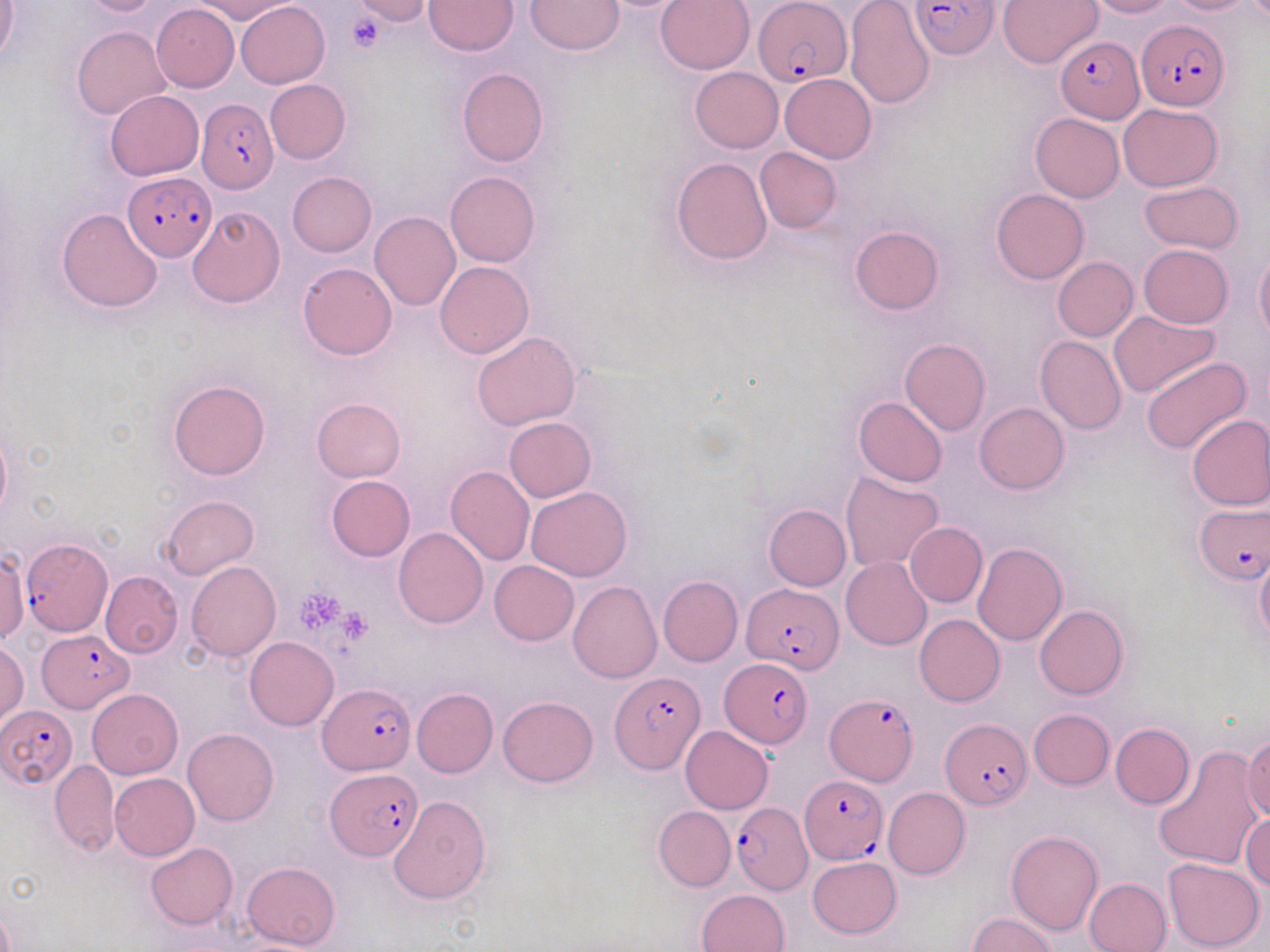

Summary:
  - Coordinate format: approximate bounding boxes as named x1/y1/x2/y2 corners in pixels
  - Platelet locations: (x1=346, y1=11, x2=389, y2=51), (x1=298, y1=591, x2=348, y2=633), (x1=336, y1=609, x2=374, y2=643)
  - Plasmodium falciparum-infected red blood cell locations: (x1=754, y1=1, x2=851, y2=88), (x1=911, y1=1, x2=999, y2=60), (x1=1135, y1=19, x2=1228, y2=113), (x1=1056, y1=36, x2=1142, y2=123), (x1=197, y1=97, x2=277, y2=194), (x1=124, y1=171, x2=217, y2=259), (x1=1194, y1=504, x2=1268, y2=583), (x1=20, y1=538, x2=113, y2=637), (x1=742, y1=582, x2=843, y2=671), (x1=39, y1=631, x2=132, y2=712), (x1=719, y1=658, x2=812, y2=749), (x1=610, y1=672, x2=704, y2=772), (x1=319, y1=682, x2=413, y2=774), (x1=825, y1=693, x2=917, y2=786), (x1=3, y1=705, x2=77, y2=786), (x1=941, y1=718, x2=1031, y2=809), (x1=326, y1=768, x2=421, y2=858), (x1=799, y1=775, x2=888, y2=864), (x1=730, y1=802, x2=812, y2=895)
  - Uninfected red blood cell locations: (x1=75, y1=0, x2=163, y2=16), (x1=193, y1=0, x2=298, y2=22), (x1=347, y1=0, x2=432, y2=26), (x1=425, y1=0, x2=518, y2=55), (x1=526, y1=0, x2=623, y2=54), (x1=656, y1=0, x2=754, y2=74), (x1=845, y1=0, x2=933, y2=107), (x1=1085, y1=0, x2=1178, y2=18), (x1=1164, y1=0, x2=1257, y2=15), (x1=998, y1=1, x2=1102, y2=70), (x1=236, y1=2, x2=330, y2=88), (x1=0, y1=3, x2=20, y2=63), (x1=151, y1=3, x2=239, y2=91), (x1=72, y1=26, x2=171, y2=121), (x1=689, y1=67, x2=783, y2=153), (x1=457, y1=68, x2=548, y2=166), (x1=781, y1=74, x2=876, y2=163), (x1=264, y1=79, x2=350, y2=164), (x1=105, y1=90, x2=204, y2=180), (x1=1118, y1=104, x2=1222, y2=191), (x1=1030, y1=112, x2=1124, y2=201), (x1=755, y1=147, x2=841, y2=232), (x1=671, y1=157, x2=773, y2=264), (x1=287, y1=171, x2=376, y2=256), (x1=445, y1=171, x2=540, y2=267), (x1=1138, y1=180, x2=1245, y2=253), (x1=991, y1=188, x2=1089, y2=285), (x1=187, y1=205, x2=284, y2=308), (x1=57, y1=207, x2=164, y2=312), (x1=371, y1=211, x2=461, y2=311), (x1=849, y1=226, x2=943, y2=315), (x1=1139, y1=245, x2=1233, y2=329), (x1=1255, y1=250, x2=1270, y2=346), (x1=1052, y1=257, x2=1139, y2=341), (x1=435, y1=261, x2=534, y2=357), (x1=297, y1=263, x2=396, y2=360), (x1=1109, y1=311, x2=1220, y2=398), (x1=472, y1=332, x2=582, y2=430), (x1=1036, y1=334, x2=1127, y2=435), (x1=899, y1=338, x2=992, y2=435), (x1=1141, y1=357, x2=1252, y2=454), (x1=168, y1=379, x2=269, y2=480), (x1=853, y1=396, x2=948, y2=486), (x1=312, y1=398, x2=406, y2=482), (x1=975, y1=402, x2=1069, y2=494), (x1=1185, y1=414, x2=1270, y2=512), (x1=505, y1=417, x2=595, y2=501), (x1=0, y1=425, x2=11, y2=522), (x1=445, y1=465, x2=534, y2=565), (x1=839, y1=471, x2=944, y2=572), (x1=325, y1=475, x2=415, y2=562), (x1=526, y1=486, x2=632, y2=581), (x1=161, y1=495, x2=257, y2=578), (x1=763, y1=504, x2=850, y2=590), (x1=904, y1=522, x2=987, y2=607), (x1=393, y1=527, x2=488, y2=628), (x1=974, y1=542, x2=1067, y2=646), (x1=1, y1=549, x2=30, y2=643), (x1=1255, y1=551, x2=1270, y2=647), (x1=841, y1=556, x2=932, y2=649), (x1=489, y1=560, x2=579, y2=646), (x1=186, y1=561, x2=281, y2=660), (x1=100, y1=571, x2=183, y2=658), (x1=657, y1=576, x2=743, y2=666), (x1=568, y1=580, x2=662, y2=683), (x1=1034, y1=605, x2=1128, y2=699), (x1=914, y1=614, x2=1005, y2=706), (x1=245, y1=636, x2=338, y2=730), (x1=0, y1=640, x2=29, y2=729), (x1=411, y1=688, x2=497, y2=778), (x1=87, y1=689, x2=183, y2=779), (x1=497, y1=696, x2=598, y2=787), (x1=1028, y1=708, x2=1114, y2=789), (x1=1110, y1=723, x2=1194, y2=809), (x1=680, y1=725, x2=773, y2=814), (x1=183, y1=727, x2=278, y2=826), (x1=1244, y1=737, x2=1270, y2=822), (x1=1153, y1=744, x2=1263, y2=871), (x1=50, y1=760, x2=120, y2=855), (x1=110, y1=773, x2=199, y2=860), (x1=882, y1=787, x2=970, y2=879), (x1=388, y1=795, x2=490, y2=905), (x1=653, y1=806, x2=734, y2=891), (x1=1242, y1=810, x2=1269, y2=894), (x1=1006, y1=830, x2=1103, y2=935), (x1=145, y1=842, x2=239, y2=929), (x1=807, y1=855, x2=901, y2=940), (x1=1163, y1=857, x2=1265, y2=951), (x1=242, y1=860, x2=340, y2=950), (x1=1083, y1=877, x2=1172, y2=952), (x1=696, y1=889, x2=790, y2=952), (x1=967, y1=913, x2=1057, y2=952)
  - Slide-level diagnosis: Plasmodium falciparum
  - Modality: optical microscopy
  - Preparation: thin blood film
  - Field of view: one of a larger specimen
  - Magnification: 1000x
  - Image size: 1270×952 pixels
  - Stain: May-Grünwald-Giemsa